Report the malaria status of this cell.
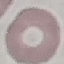
It is uninfected.

Summary:
  - Stain: Giemsa
  - Image type: cell patch, automatically extracted from a larger field of view and resized to 64 × 64 pixels
  - Capture: smartphone camera at the microscope eyepiece
  - Preparation: thin blood smear